Classify this cell by malaria status.
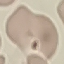

Uninfected.

Giemsa stain. Automatically extracted cell patch, resized to 64 × 64 pixels. Thin blood film. Acquired by smartphone through the microscope eyepiece.